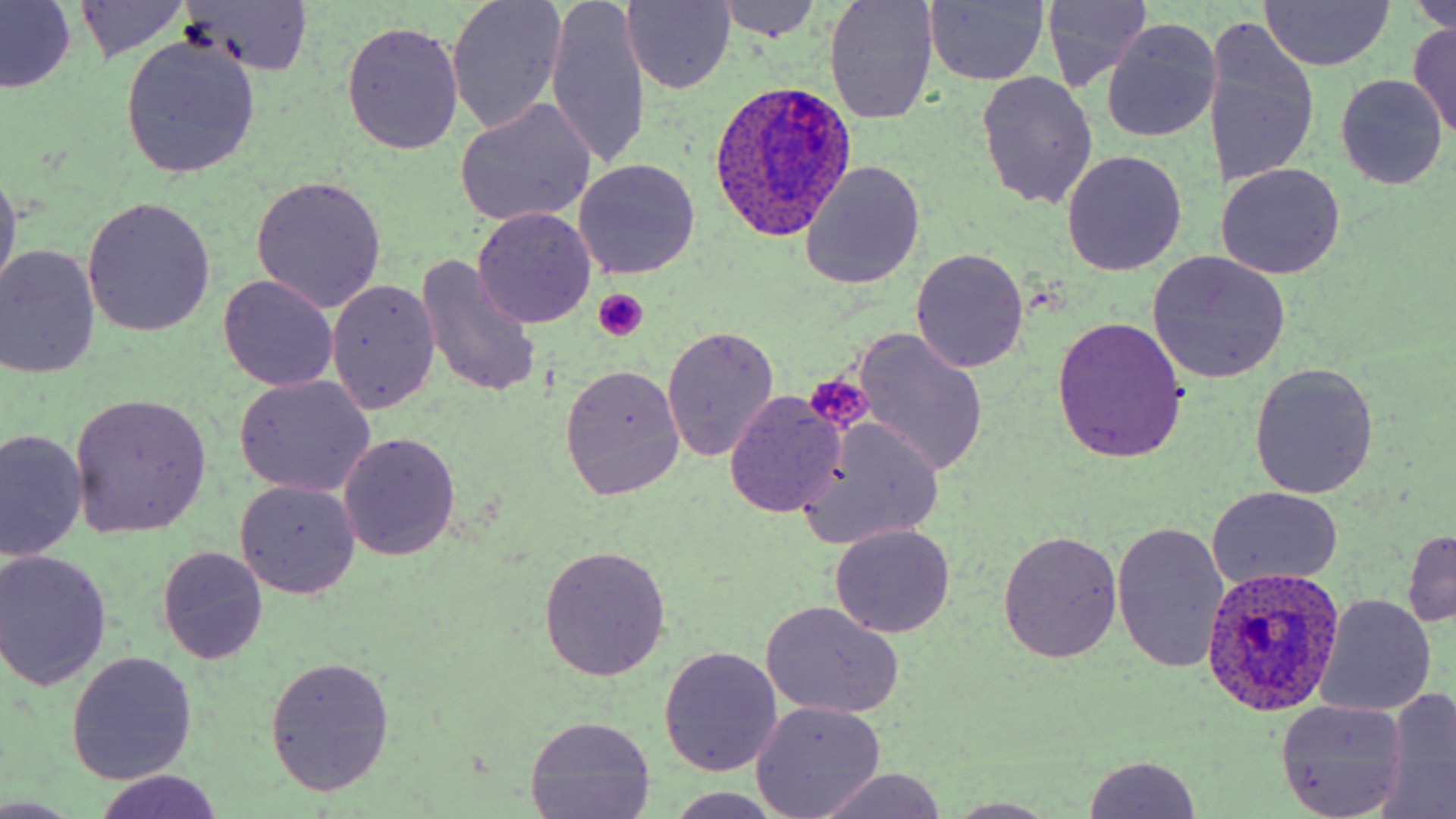
Summary:
  - Coordinate format: approximate bounding boxes as named x1/y1/x2/y2 corners in pixels
  - Platelet locations: (x1=592, y1=288, x2=650, y2=340), (x1=805, y1=372, x2=872, y2=436)
  - Uninfected red blood cell locations: (x1=0, y1=0, x2=78, y2=94), (x1=447, y1=0, x2=566, y2=133), (x1=546, y1=0, x2=649, y2=172), (x1=1412, y1=0, x2=1456, y2=36), (x1=70, y1=1, x2=191, y2=63), (x1=177, y1=1, x2=314, y2=77), (x1=622, y1=1, x2=736, y2=92), (x1=711, y1=1, x2=825, y2=43), (x1=824, y1=1, x2=941, y2=124), (x1=924, y1=1, x2=1051, y2=86), (x1=1258, y1=1, x2=1395, y2=71), (x1=1040, y1=3, x2=1152, y2=90), (x1=1101, y1=19, x2=1223, y2=142), (x1=1203, y1=20, x2=1322, y2=194), (x1=1406, y1=20, x2=1456, y2=139), (x1=341, y1=22, x2=464, y2=156), (x1=119, y1=38, x2=259, y2=178), (x1=976, y1=70, x2=1099, y2=211), (x1=1337, y1=74, x2=1448, y2=190), (x1=455, y1=100, x2=596, y2=227), (x1=1062, y1=151, x2=1186, y2=276), (x1=574, y1=158, x2=699, y2=280), (x1=799, y1=161, x2=926, y2=289), (x1=1216, y1=162, x2=1345, y2=279), (x1=0, y1=166, x2=21, y2=304), (x1=251, y1=176, x2=387, y2=312), (x1=83, y1=199, x2=216, y2=337), (x1=473, y1=208, x2=597, y2=329), (x1=0, y1=247, x2=101, y2=380), (x1=912, y1=248, x2=1027, y2=371), (x1=1148, y1=253, x2=1289, y2=382), (x1=415, y1=259, x2=541, y2=399), (x1=218, y1=274, x2=339, y2=393), (x1=327, y1=279, x2=441, y2=415), (x1=1050, y1=316, x2=1189, y2=460), (x1=662, y1=325, x2=778, y2=463), (x1=849, y1=329, x2=988, y2=478), (x1=559, y1=363, x2=685, y2=501), (x1=1250, y1=363, x2=1379, y2=500), (x1=233, y1=376, x2=375, y2=498), (x1=725, y1=390, x2=848, y2=517), (x1=70, y1=393, x2=212, y2=538), (x1=796, y1=419, x2=947, y2=550), (x1=1, y1=431, x2=85, y2=560), (x1=338, y1=433, x2=461, y2=560), (x1=235, y1=481, x2=361, y2=599), (x1=1207, y1=486, x2=1345, y2=589), (x1=1111, y1=520, x2=1230, y2=673), (x1=829, y1=524, x2=953, y2=637), (x1=1403, y1=530, x2=1456, y2=628), (x1=998, y1=531, x2=1124, y2=665), (x1=158, y1=546, x2=267, y2=664), (x1=538, y1=546, x2=672, y2=680), (x1=785, y1=549, x2=946, y2=691), (x1=0, y1=551, x2=112, y2=689), (x1=1315, y1=595, x2=1435, y2=716), (x1=760, y1=600, x2=905, y2=719), (x1=660, y1=647, x2=783, y2=775), (x1=67, y1=653, x2=197, y2=784), (x1=266, y1=656, x2=394, y2=797), (x1=1379, y1=689, x2=1456, y2=814), (x1=1274, y1=700, x2=1407, y2=818), (x1=751, y1=701, x2=886, y2=817), (x1=525, y1=716, x2=658, y2=817), (x1=1080, y1=755, x2=1204, y2=819), (x1=811, y1=768, x2=949, y2=819), (x1=93, y1=770, x2=223, y2=819), (x1=666, y1=789, x2=786, y2=819), (x1=0, y1=796, x2=77, y2=817), (x1=944, y1=798, x2=1062, y2=818)
  - Plasmodium ovale-infected red blood cell locations: (x1=715, y1=84, x2=851, y2=238), (x1=1201, y1=563, x2=1345, y2=717)
  - Slide-level diagnosis: Plasmodium ovale
  - Preparation: thin blood smear
  - Magnification: 1000x
  - Modality: light microscopy
  - Image size: 1456×819 pixels
  - Stain: May-Grünwald-Giemsa
  - Field of view: one of a larger specimen